Classify this cell by malaria status.
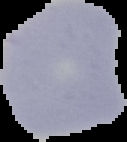

Uninfected.

Image is 127×142 pixels. From a thin blood film. The area outside the segmented cell region is set to black.